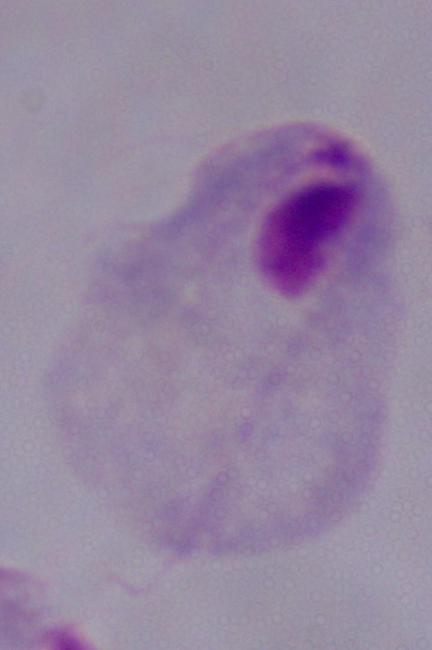
Photomicrograph. A trichomonad is seen. 1000x magnification.